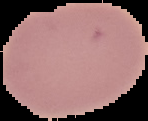

Summary:
  - Preparation: thin blood film
  - Image type: segmented cell region with the area outside set to black
  - Malaria status: uninfected
  - Image size: 148×121 pixels